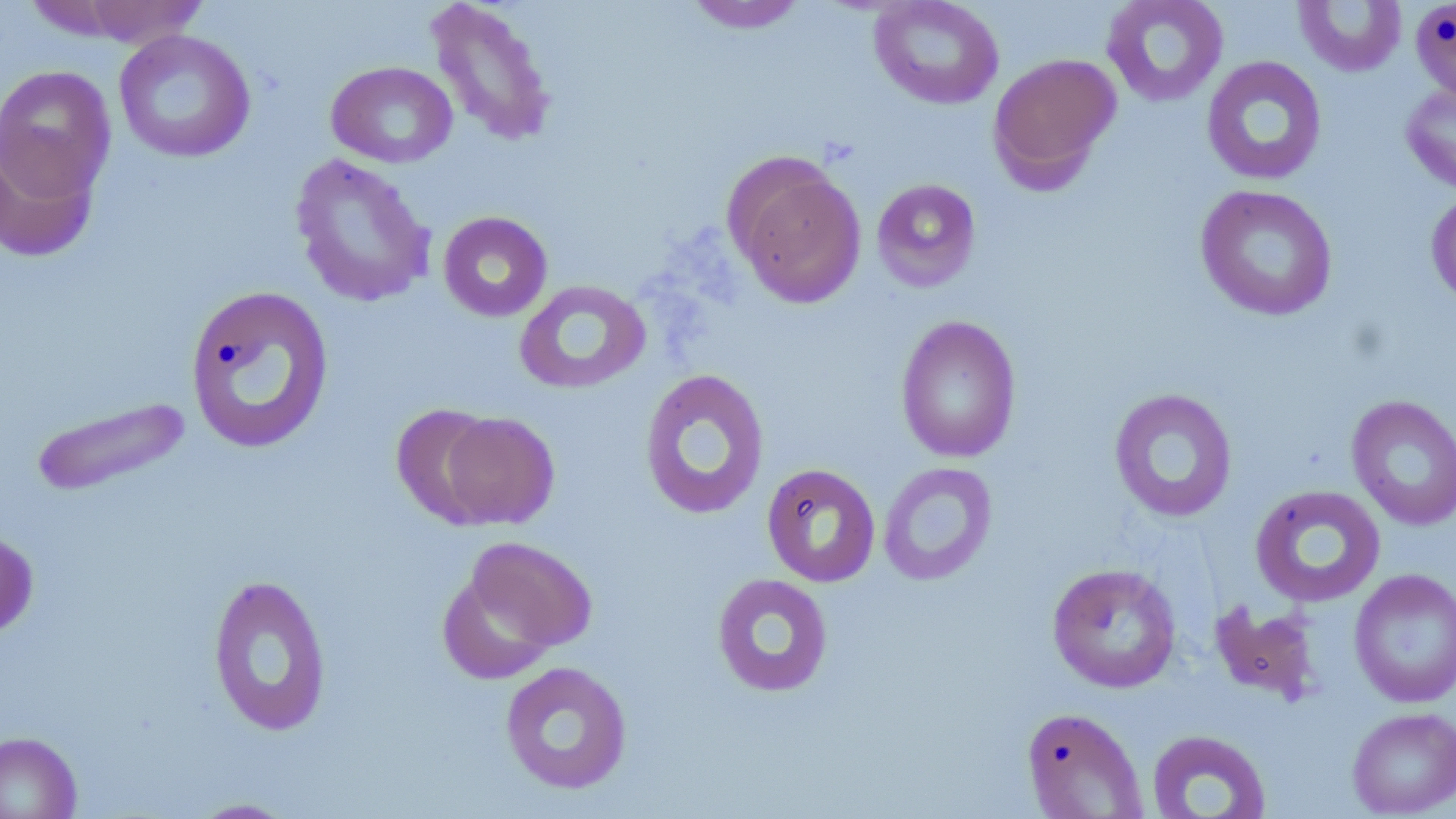
slide-level diagnosis = no evidence of blood parasites
uninfected red blood cell locations = approximate bounding boxes as [x1, y1, x2, y2] in pixels: [425, 0, 558, 148], [868, 0, 1005, 110], [1101, 0, 1229, 108], [1410, 0, 1456, 103], [71, 1, 210, 47], [683, 1, 809, 34], [1293, 1, 1407, 77], [113, 29, 256, 164], [987, 53, 1121, 190], [1200, 55, 1328, 186], [326, 60, 458, 168], [0, 65, 117, 201], [1401, 81, 1456, 196], [0, 133, 101, 264], [289, 153, 437, 309], [729, 158, 867, 309], [871, 178, 982, 292], [1195, 184, 1339, 322], [1426, 189, 1456, 308], [437, 211, 553, 322], [513, 279, 652, 396], [184, 284, 335, 455], [895, 314, 1022, 464], [638, 367, 770, 520], [1108, 387, 1238, 523], [1346, 395, 1456, 531], [30, 396, 194, 498], [391, 404, 503, 528], [436, 412, 560, 529], [877, 461, 998, 586], [761, 462, 881, 587], [1249, 484, 1386, 608], [0, 529, 39, 640], [460, 536, 599, 659], [1046, 562, 1182, 693], [1348, 569, 1456, 708], [711, 572, 834, 698], [207, 573, 333, 737], [1209, 600, 1324, 705], [499, 661, 633, 795], [1021, 706, 1148, 818], [1346, 707, 1456, 817], [1145, 728, 1272, 818], [0, 730, 83, 818], [185, 797, 302, 818]
magnification = 1000x
preparation = thin blood film
stain = May-Grünwald-Giemsa
modality = light microscopy
image size = 1456×819 pixels
field of view = single